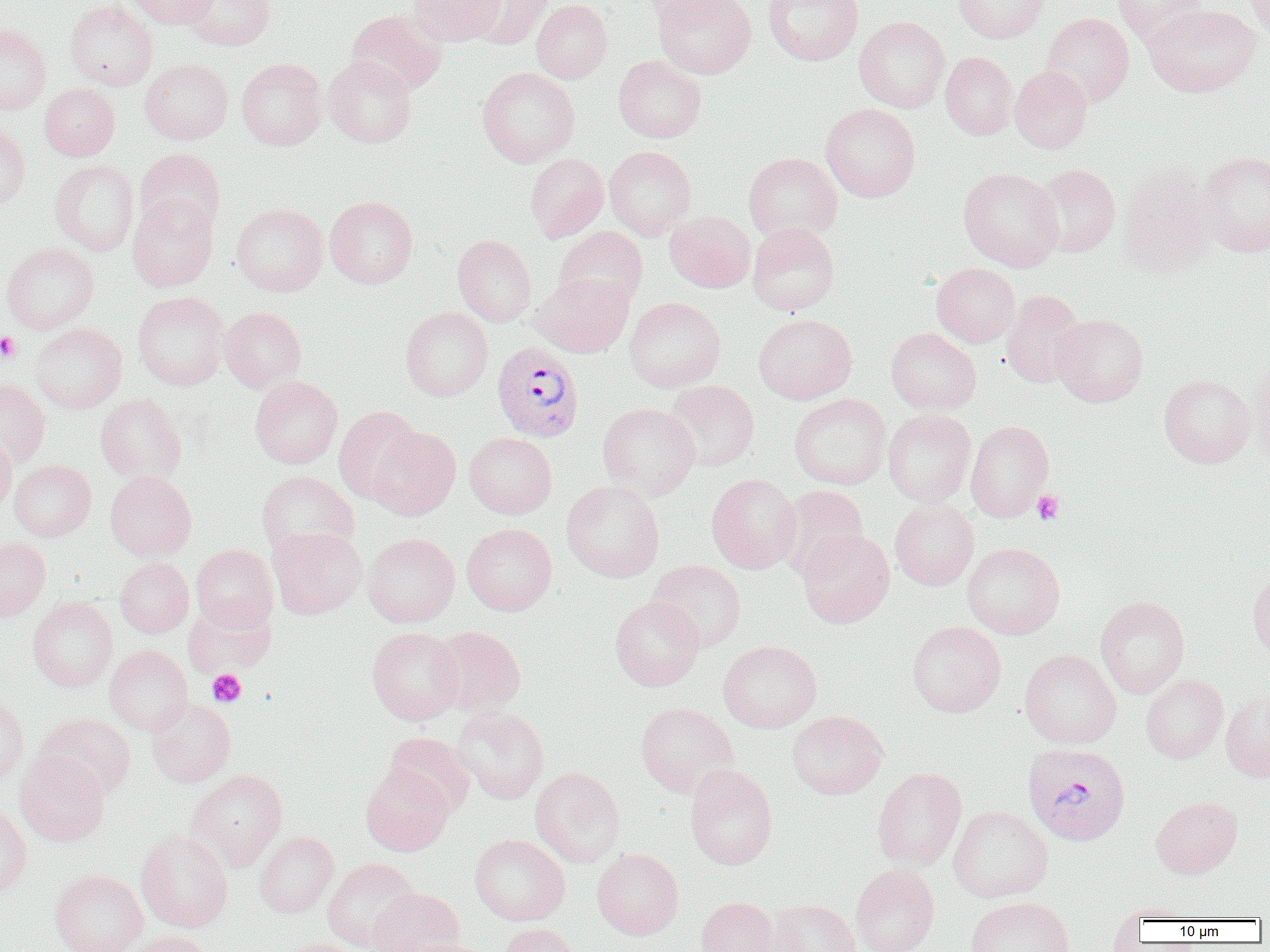

slide-level diagnosis = Plasmodium vivax
magnification = 1000x
image size = 1270×952 pixels
modality = light microscopy
Plasmodium vivax-infected red blood cell locations = approximate bounding boxes as named x1/y1/x2/y2 corners in pixels: (x1=492, y1=342, x2=584, y2=441), (x1=1022, y1=742, x2=1130, y2=846)
platelet locations = approximate bounding boxes as named x1/y1/x2/y2 corners in pixels: (x1=0, y1=332, x2=21, y2=363), (x1=1032, y1=490, x2=1064, y2=525), (x1=207, y1=669, x2=246, y2=707)
uninfected red blood cell locations = approximate bounding boxes as named x1/y1/x2/y2 corners in pixels: (x1=64, y1=0, x2=157, y2=90), (x1=124, y1=0, x2=219, y2=28), (x1=181, y1=0, x2=275, y2=50), (x1=409, y1=0, x2=504, y2=46), (x1=464, y1=0, x2=551, y2=49), (x1=531, y1=0, x2=612, y2=83), (x1=638, y1=0, x2=737, y2=21), (x1=653, y1=0, x2=755, y2=78), (x1=763, y1=0, x2=864, y2=66), (x1=954, y1=0, x2=1050, y2=43), (x1=1112, y1=0, x2=1207, y2=46), (x1=1245, y1=0, x2=1270, y2=42), (x1=1144, y1=3, x2=1261, y2=97), (x1=345, y1=9, x2=447, y2=95), (x1=1041, y1=12, x2=1134, y2=107), (x1=854, y1=16, x2=950, y2=113), (x1=0, y1=24, x2=51, y2=114), (x1=940, y1=51, x2=1017, y2=139), (x1=613, y1=55, x2=707, y2=142), (x1=323, y1=56, x2=417, y2=147), (x1=237, y1=57, x2=327, y2=151), (x1=140, y1=58, x2=233, y2=144), (x1=1010, y1=66, x2=1093, y2=153), (x1=477, y1=67, x2=580, y2=167), (x1=39, y1=83, x2=120, y2=161), (x1=821, y1=103, x2=920, y2=202), (x1=0, y1=124, x2=30, y2=212), (x1=604, y1=146, x2=696, y2=239), (x1=134, y1=148, x2=226, y2=236), (x1=1198, y1=151, x2=1270, y2=256), (x1=743, y1=152, x2=842, y2=243), (x1=525, y1=153, x2=608, y2=242), (x1=50, y1=159, x2=140, y2=256), (x1=1033, y1=164, x2=1120, y2=257), (x1=1118, y1=164, x2=1218, y2=276), (x1=958, y1=167, x2=1063, y2=271), (x1=127, y1=195, x2=219, y2=291), (x1=325, y1=195, x2=418, y2=288), (x1=232, y1=203, x2=328, y2=296), (x1=665, y1=211, x2=755, y2=292), (x1=747, y1=223, x2=839, y2=315), (x1=554, y1=226, x2=648, y2=310), (x1=452, y1=234, x2=537, y2=327), (x1=1, y1=243, x2=99, y2=334), (x1=932, y1=263, x2=1020, y2=347), (x1=534, y1=273, x2=633, y2=357), (x1=1001, y1=290, x2=1087, y2=388), (x1=132, y1=291, x2=229, y2=391), (x1=624, y1=297, x2=726, y2=392), (x1=219, y1=306, x2=306, y2=393), (x1=400, y1=306, x2=493, y2=401), (x1=753, y1=313, x2=857, y2=405), (x1=1051, y1=313, x2=1148, y2=406), (x1=30, y1=323, x2=127, y2=414), (x1=886, y1=327, x2=981, y2=414), (x1=1248, y1=359, x2=1270, y2=469), (x1=1158, y1=373, x2=1255, y2=468), (x1=250, y1=376, x2=342, y2=468), (x1=0, y1=378, x2=50, y2=468), (x1=663, y1=379, x2=759, y2=471), (x1=96, y1=393, x2=187, y2=484), (x1=789, y1=393, x2=891, y2=490), (x1=598, y1=402, x2=699, y2=500), (x1=334, y1=406, x2=422, y2=503), (x1=883, y1=409, x2=976, y2=506), (x1=965, y1=420, x2=1054, y2=521), (x1=367, y1=427, x2=460, y2=520), (x1=0, y1=430, x2=17, y2=517), (x1=464, y1=432, x2=557, y2=519), (x1=9, y1=460, x2=96, y2=541), (x1=256, y1=470, x2=359, y2=557), (x1=105, y1=471, x2=197, y2=561), (x1=706, y1=473, x2=802, y2=573), (x1=561, y1=480, x2=664, y2=583), (x1=776, y1=485, x2=869, y2=579), (x1=890, y1=497, x2=979, y2=590), (x1=462, y1=523, x2=557, y2=616), (x1=267, y1=527, x2=367, y2=619), (x1=797, y1=529, x2=894, y2=627), (x1=363, y1=532, x2=459, y2=627), (x1=0, y1=536, x2=51, y2=621), (x1=962, y1=542, x2=1064, y2=639), (x1=191, y1=544, x2=279, y2=632), (x1=114, y1=558, x2=194, y2=637), (x1=646, y1=560, x2=747, y2=651), (x1=1247, y1=568, x2=1270, y2=662), (x1=1095, y1=595, x2=1190, y2=697), (x1=610, y1=596, x2=704, y2=691), (x1=28, y1=597, x2=117, y2=691), (x1=184, y1=601, x2=271, y2=676), (x1=907, y1=621, x2=1006, y2=717), (x1=367, y1=626, x2=463, y2=725), (x1=430, y1=626, x2=525, y2=716), (x1=718, y1=640, x2=822, y2=732), (x1=105, y1=644, x2=193, y2=735), (x1=1019, y1=649, x2=1121, y2=748), (x1=1141, y1=674, x2=1228, y2=764), (x1=1221, y1=690, x2=1270, y2=783), (x1=0, y1=696, x2=29, y2=785), (x1=146, y1=698, x2=235, y2=787), (x1=635, y1=702, x2=738, y2=798), (x1=450, y1=706, x2=550, y2=803), (x1=787, y1=711, x2=888, y2=799), (x1=35, y1=713, x2=136, y2=799), (x1=383, y1=732, x2=475, y2=817), (x1=15, y1=751, x2=110, y2=846), (x1=685, y1=764, x2=778, y2=870), (x1=361, y1=765, x2=454, y2=855), (x1=530, y1=767, x2=625, y2=867), (x1=871, y1=767, x2=966, y2=872), (x1=187, y1=769, x2=287, y2=870), (x1=1150, y1=795, x2=1242, y2=878), (x1=0, y1=804, x2=32, y2=898), (x1=948, y1=805, x2=1053, y2=902), (x1=135, y1=830, x2=233, y2=932), (x1=254, y1=831, x2=338, y2=918), (x1=469, y1=834, x2=569, y2=925), (x1=592, y1=848, x2=683, y2=940), (x1=322, y1=857, x2=421, y2=952), (x1=850, y1=864, x2=940, y2=952), (x1=49, y1=869, x2=147, y2=952), (x1=368, y1=888, x2=464, y2=952), (x1=965, y1=896, x2=1074, y2=952), (x1=696, y1=897, x2=780, y2=952), (x1=769, y1=899, x2=860, y2=952), (x1=1110, y1=903, x2=1201, y2=923), (x1=500, y1=923, x2=582, y2=952), (x1=124, y1=931, x2=215, y2=952), (x1=274, y1=938, x2=367, y2=952), (x1=401, y1=939, x2=496, y2=952)
preparation = thin blood smear
field of view = single